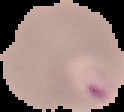

image size = 124×112 pixels
preparation = thin blood film
result = malaria parasites identified
image type = segmented cell region with the area outside set to black